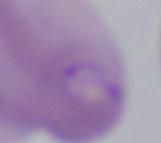
Summary:
  - Magnification: 1000x
  - Modality: photomicrograph
  - Identification: Babesia